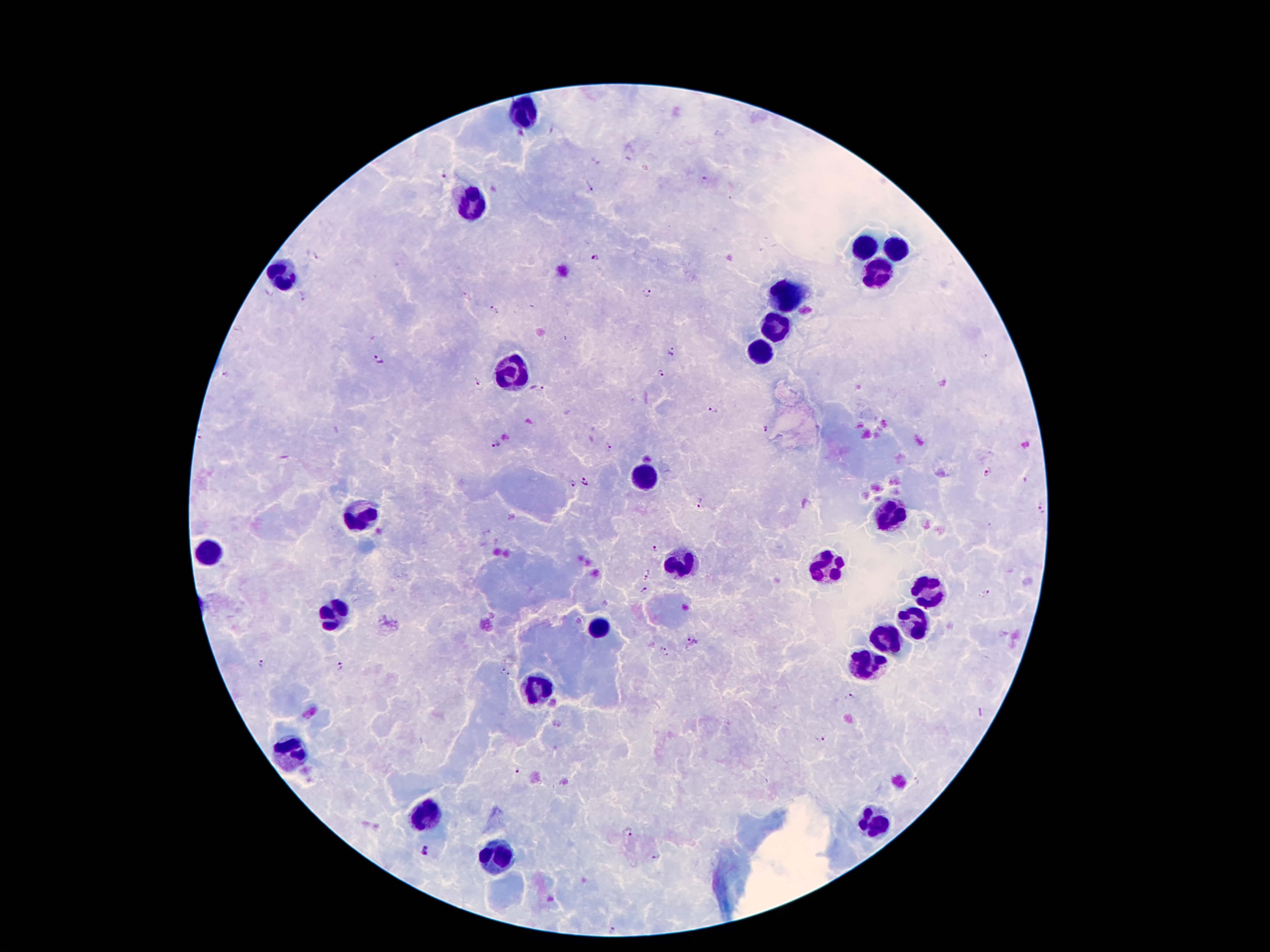

Approximate centers as {x, y} in pixels. Plasmodium parasite locations: {445, 174}, {706, 177}, {589, 189}, {318, 256}, {595, 258}, {647, 291}, {302, 295}, {495, 308}, {673, 352}, {379, 358}, {661, 371}, {225, 373}, {478, 381}, {538, 387}, {713, 411}, {763, 428}, {496, 443}, {610, 445}, {987, 475}, {585, 480}, {572, 484}, {699, 501}, {1041, 510}, {654, 549}, {646, 576}, {642, 591}, {984, 594}, {692, 643}, {664, 647}, {262, 664}, {340, 665}, {506, 675}, {850, 697}, {820, 738}, {519, 772}, {630, 835}, {425, 849}, {655, 855}, {613, 929}. Leukocyte locations: {526, 115}, {474, 205}, {868, 247}, {896, 247}, {285, 274}, {877, 277}, {787, 296}, {778, 327}, {763, 352}, {509, 373}, {646, 476}, {892, 514}, {362, 516}, {209, 550}, {682, 562}, {831, 566}, {929, 590}, {335, 613}, {600, 627}, {912, 627}, {889, 640}, {868, 663}, {537, 690}, {293, 749}, {428, 816}, {873, 823}, {495, 858}. Patient malaria status: infected with Plasmodium falciparum. Image is 1270×952 pixels. One field from this slide. Giemsa-stained preparation. Smartphone photograph taken through the microscope eyepiece. 100x magnification. Thick blood smear.